Classify this cell by malaria status.
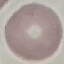
It is uninfected.

Giemsa stain. Thin smear of blood. Acquired by smartphone through the microscope eyepiece. Cell patch, automatically extracted from a larger field of view and resized to 64 × 64 pixels.